Comment on the morphology of the red blood cells.
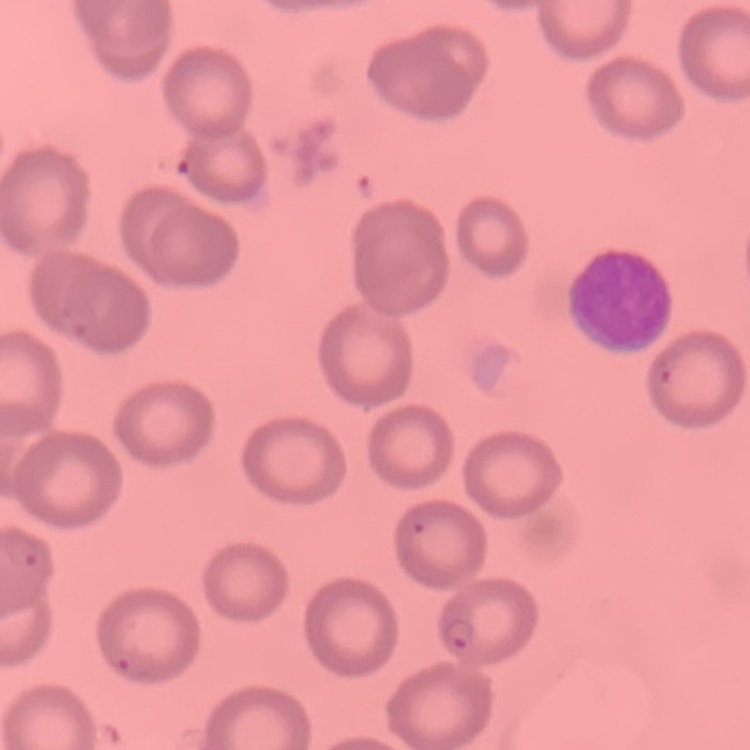

No rouleaux formation.

image type = one tile cut from a larger photomicrograph
preparation = thin peripheral smear
stain = Field's or Giemsa